State which parasite is depicted.
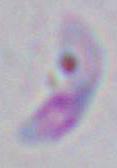
This is Toxoplasma gondii.

Summary:
  - Modality: micrograph
  - Magnification: 1000x